Locate and identify every blood parasite.
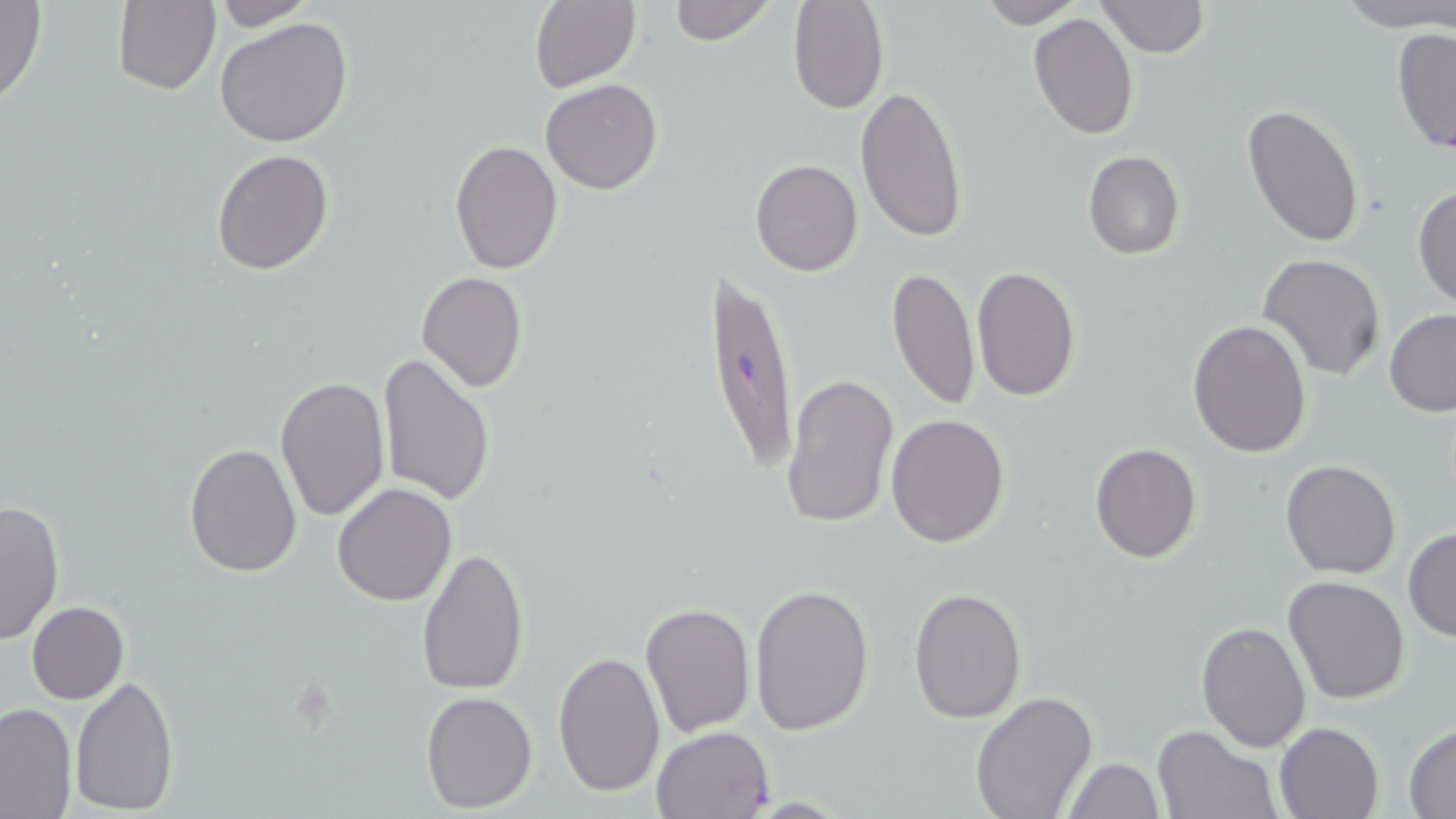

Approximate bounding boxes as (x1,y1)-(x2,y2) corner pairs in pixels.
Plasmodium falciparum-infected red blood cells: (700,257)-(799,479).
No Plasmodium ovale, Plasmodium malariae, Plasmodium vivax, Babesia divergens, or Trypanosoma brucei observed.

Summary:
  - Uninfected red blood cell locations: (0,0)-(48,107), (530,0)-(641,93), (666,0)-(775,46), (789,0)-(889,114), (1096,0)-(1207,57), (1339,0)-(1456,31), (112,1)-(219,95), (211,1)-(315,29), (974,1)-(1083,27), (1028,13)-(1139,139), (213,17)-(354,148), (1393,26)-(1456,158), (541,78)-(663,196), (856,84)-(969,243), (1242,104)-(1365,250), (449,139)-(562,273), (210,149)-(334,276), (1083,150)-(1184,259), (750,158)-(861,276), (1412,185)-(1456,310), (1258,253)-(1385,380), (971,264)-(1081,401), (887,266)-(979,410), (416,272)-(527,393), (1384,310)-(1456,417), (1187,319)-(1312,457), (378,354)-(496,507), (780,372)-(898,531), (275,376)-(389,521), (885,414)-(1009,549), (184,442)-(303,578), (1089,443)-(1202,563), (1280,459)-(1401,580), (332,483)-(457,606), (0,498)-(64,648), (1404,528)-(1456,642), (416,545)-(529,696), (1281,575)-(1410,705), (749,580)-(874,736), (909,586)-(1027,725), (26,601)-(129,704), (639,603)-(755,736), (1195,621)-(1311,754), (552,651)-(665,797), (69,674)-(178,815), (421,690)-(537,810), (970,691)-(1099,818), (0,702)-(75,817), (1275,721)-(1384,819), (1405,724)-(1456,817), (1152,725)-(1279,819), (650,726)-(774,818), (1064,756)-(1164,819)
  - Slide-level diagnosis: Plasmodium falciparum
  - Magnification: 1000x
  - Modality: light microscopy
  - Preparation: thin blood film
  - Field of view: one of a larger specimen
  - Image size: 1456×819 pixels
  - Stain: May-Grünwald-Giemsa